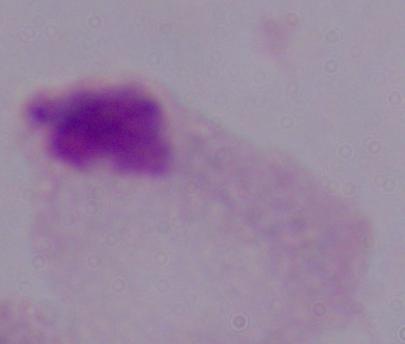
Captured at 1000x magnification. A trichomonad is seen. Micrograph.